Comment on the morphology of the erythrocytes.
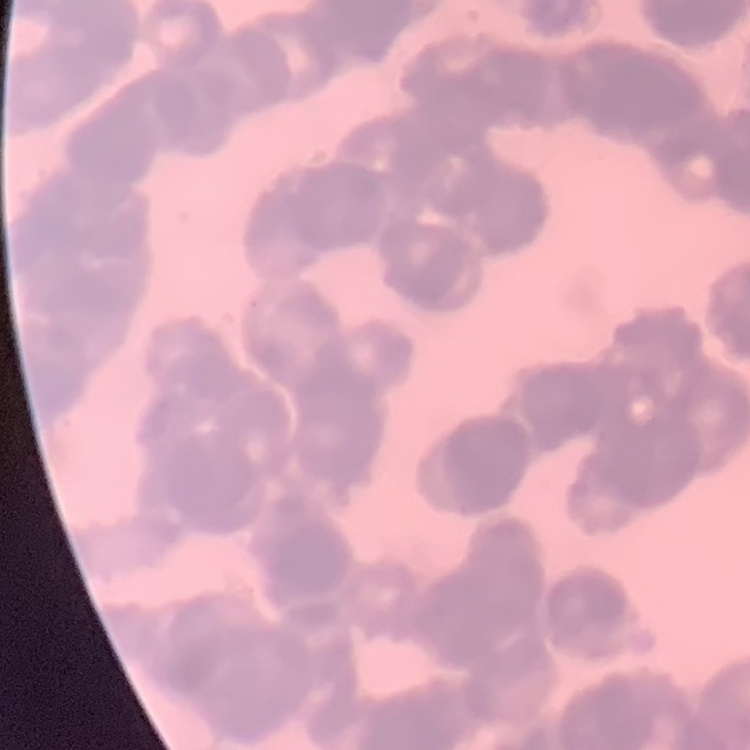

Rouleaux formation.

Summary:
  - Preparation: thin blood smear
  - Stain: Field's or Giemsa
  - Image type: one tile cut from a larger photomicrograph